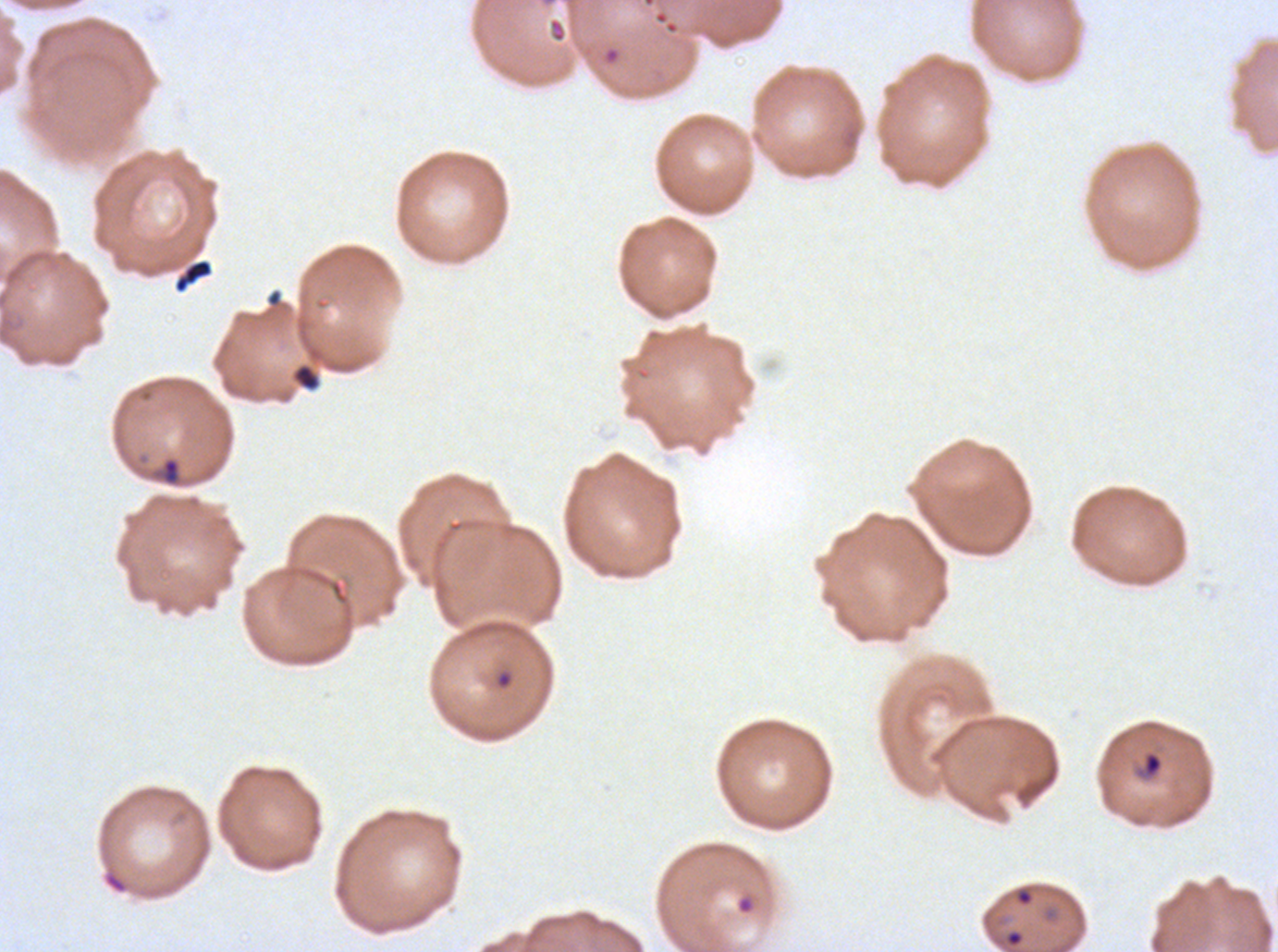

Approximate bounding boxes as (x1, y1, x2, y2) in pixels. Debris locations: (173, 258, 214, 294), (293, 364, 320, 391). Ring locations: (161, 457, 181, 486), (1134, 750, 1164, 780), (1014, 886, 1035, 907), (736, 895, 755, 915). A sub-image separated from a larger composite. Thin blood smear. Ex-vivo P. falciparum culture from a patient in The Gambia, grown for 24 to 48 hours. Image is 1278×952 pixels. Giemsa stain.